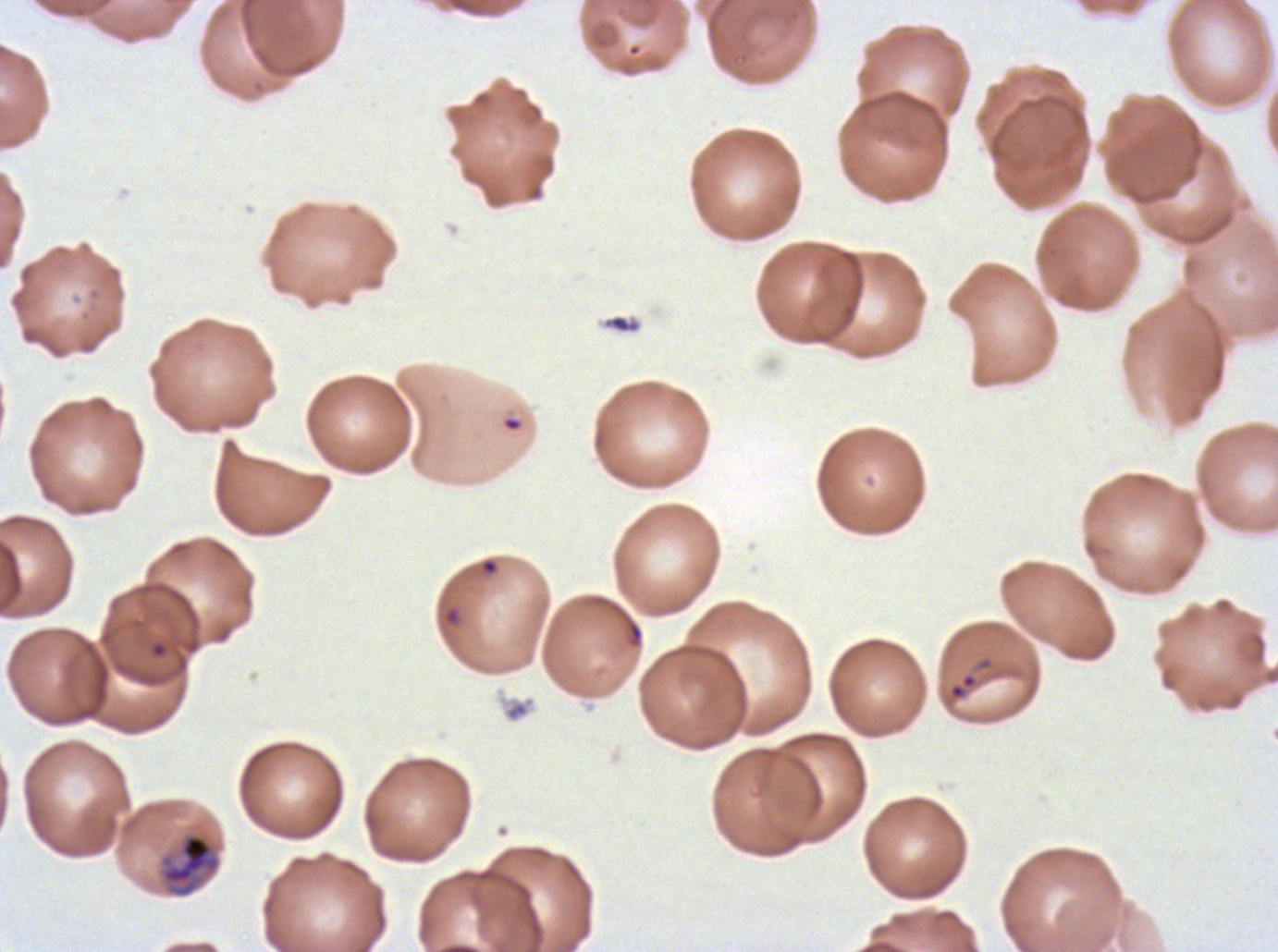
notation = approximate bounding boxes as [x1, y1, x2, y2] in pixels
mid trophozoite locations = [158, 831, 221, 898]
ring locations = [150, 641, 167, 658], [949, 673, 977, 700]
preparation = thin blood smear
field of view = sub-image separated from a larger composite
specimen = Plasmodium falciparum cultured ex vivo for 24 to 48 hours, from a patient in The Gambia
life-cycle stages observed = ring, mid trophozoite
stain = Giemsa
image size = 1278×952 pixels